Classify this cell by malaria status.
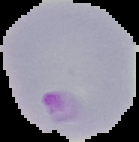
It is parasitized.

Summary:
  - Image type: segmented cell region on a black background
  - Preparation: thin blood film
  - Image size: 139×142 pixels